Classify this cell by malaria status.
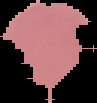

It is uninfected.

Summary:
  - Preparation: thin blood smear
  - Image type: cell region segmented out of the field of view; surrounding area masked to black
  - Image size: 97×103 pixels